Classify this cell by malaria status.
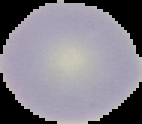

It is uninfected.

Segmented cell region on a black background. From a thin blood smear. Image is 142×124 pixels.